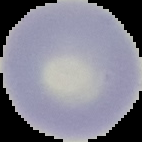

Summary:
  - Image type: segmented cell region with the area outside set to black
  - Image size: 142×142 pixels
  - Preparation: thin blood smear
  - Malaria status: uninfected